Assess this cell for malaria.
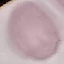

Uninfected.

Giemsa-stained preparation. Thin blood smear. Cell patch, automatically extracted from a larger field of view and resized to 64 × 64 pixels. Photographed with a smartphone camera at the microscope eyepiece.